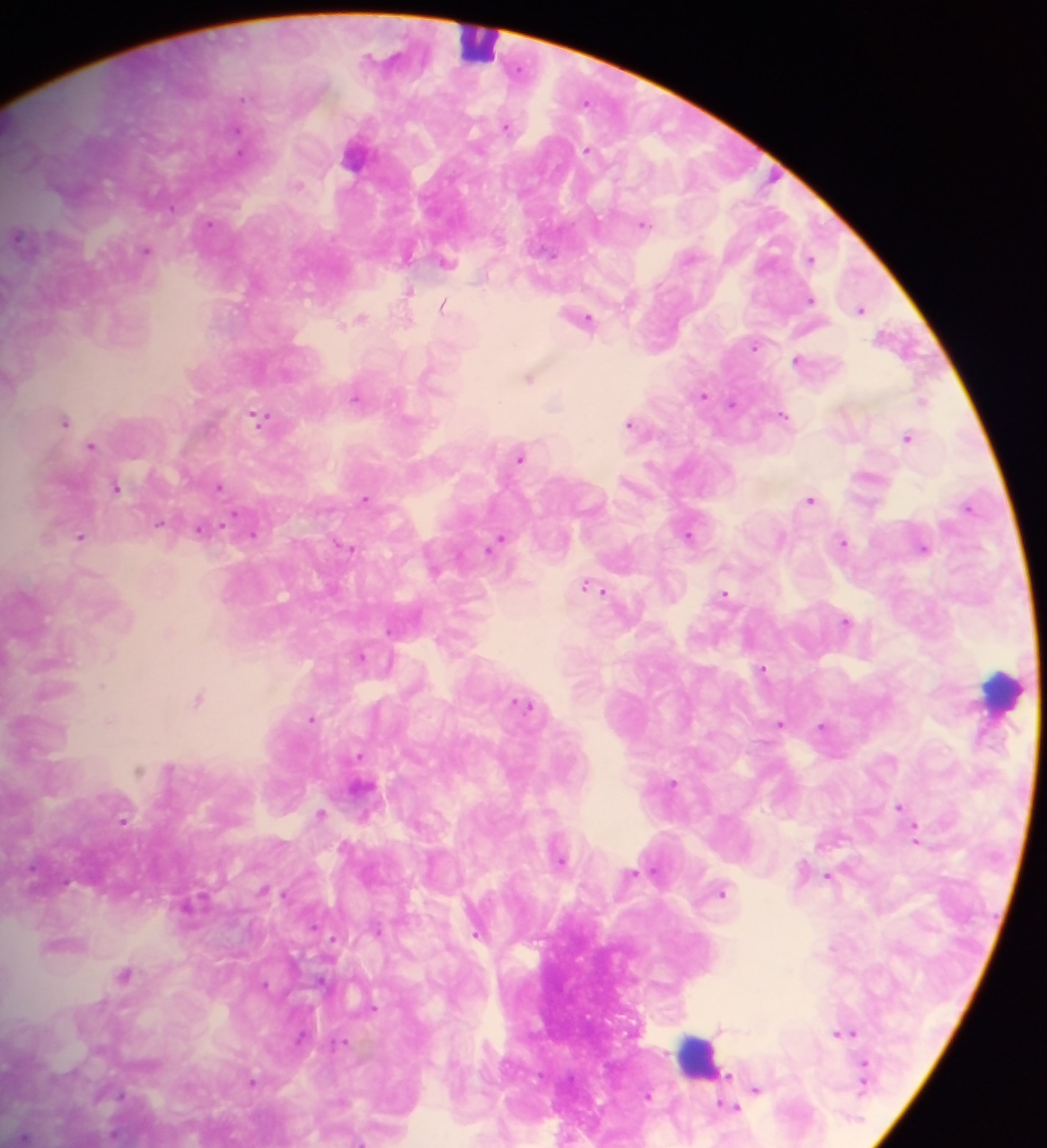
{
  "field_of_view": "single",
  "malaria_parasite_locations": "approximate centers as x y in pixels: 519 69; 244 98; 586 100; 507 126; 237 129; 588 149; 299 185; 209 224; 644 224; 18 235; 146 251; 811 259; 446 262; 409 291; 811 299; 443 305; 862 309; 361 318; 585 318; 754 346; 797 360; 530 378; 702 395; 356 397; 924 401; 732 403; 784 415; 260 419; 64 421; 630 423; 908 437; 92 445; 521 457; 115 486; 219 487; 365 498; 810 499; 969 507; 159 522; 201 529; 688 533; 253 535; 81 537; 843 542; 496 543; 924 548; 350 549; 591 586; 724 594; 846 621; 389 630; 361 656; 762 668; 101 686; 198 698; 524 705; 311 719; 109 721; 781 723; 822 726; 359 756; 672 782; 900 806; 321 814; 124 820; 917 835; 561 860; 631 873; 829 875; 723 892; 378 930; 477 934; 334 938; 125 974; 321 980; 265 985; 374 1008; 719 1027; 847 1032; 838 1033; 343 1042; 863 1064; 728 1076; 252 1081; 863 1083; 756 1089; 121 1095; 649 1095; 730 1108; 24 1136; 358 1141",
  "capture": "mobile-phone photograph through a microscope",
  "image_size": "1047×1148 pixels",
  "preparation": "thick blood film",
  "country": "Ghana",
  "leukocyte_locations": "approximate centers as x y in pixels: 476 40; 1002 690; 698 1055"
}